Assess the morphology of the erythrocytes.
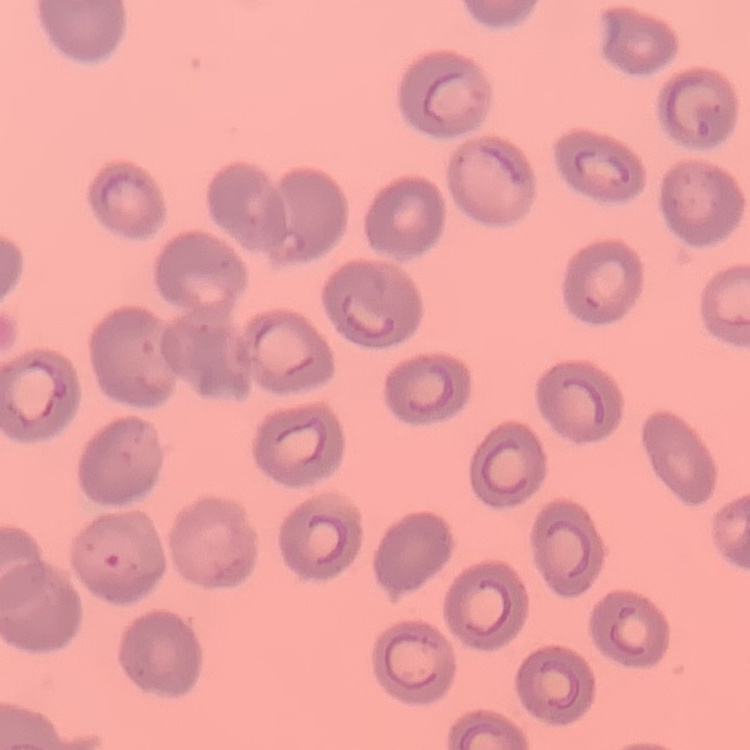

They show no rouleaux formation.

{
  "preparation": "thin peripheral smear",
  "stain": "Field's or Giemsa",
  "image_type": "square crop of a larger photomicrograph"
}